Locate every blood parasite and identify its species.
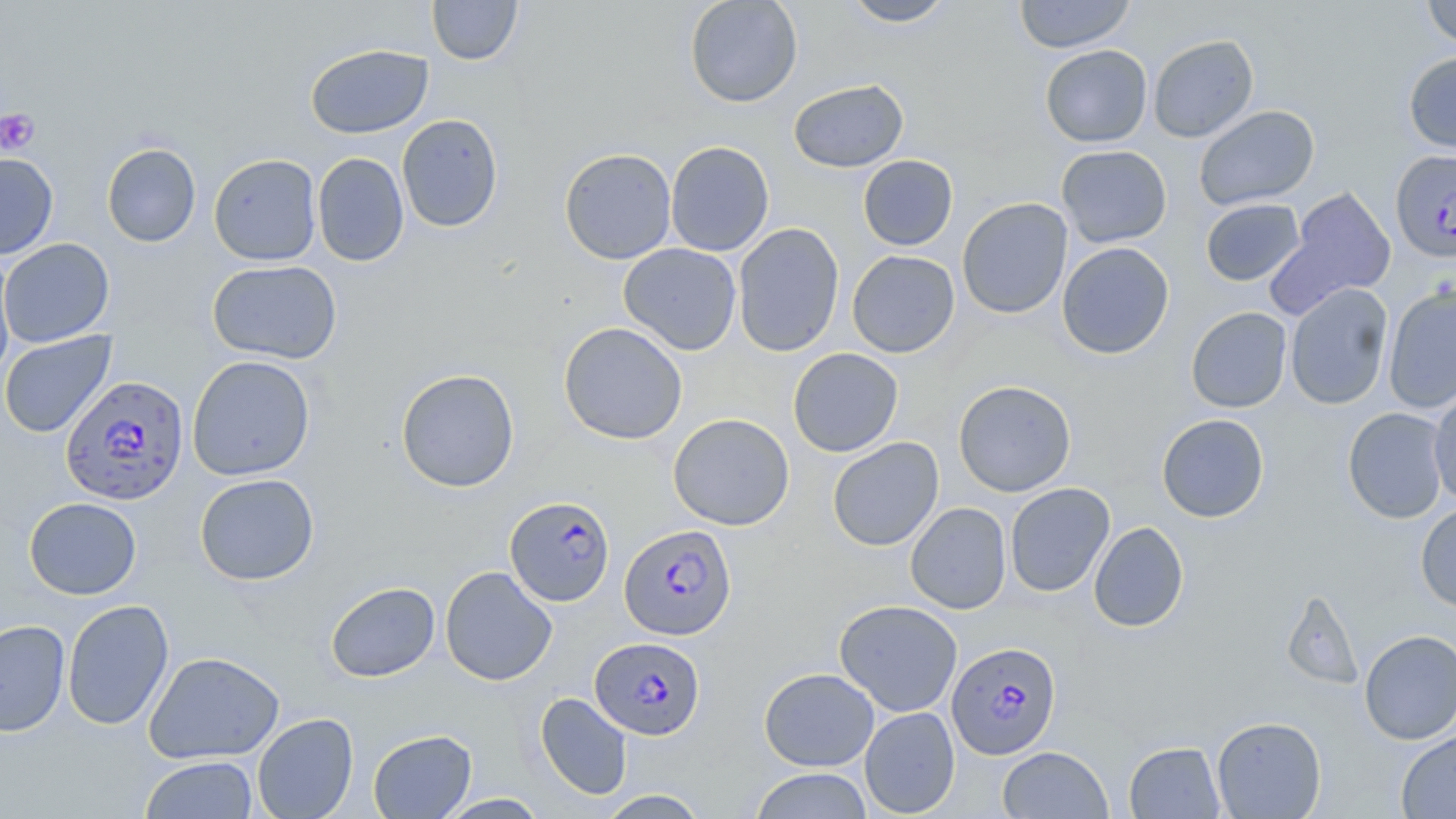
Approximate bounding boxes as [x1, y1, x2, y2] in pixels.
Plasmodium falciparum-infected red blood cells: [1390, 149, 1456, 262], [60, 374, 188, 505], [505, 495, 616, 606], [619, 524, 736, 640], [589, 638, 706, 741], [946, 641, 1062, 760].
No Plasmodium ovale, Plasmodium malariae, Plasmodium vivax, Babesia divergens, or Trypanosoma brucei observed.

Uninfected red blood cell locations: [427, 0, 523, 65], [684, 0, 803, 108], [841, 0, 957, 27], [1013, 0, 1136, 53], [1421, 0, 1456, 49], [1148, 34, 1259, 143], [304, 44, 434, 139], [1040, 44, 1152, 148], [1403, 51, 1456, 153], [788, 79, 909, 173], [1194, 105, 1320, 211], [396, 113, 504, 233], [665, 140, 775, 257], [101, 143, 201, 247], [1056, 144, 1172, 248], [559, 147, 677, 264], [0, 152, 59, 260], [312, 152, 409, 267], [208, 153, 322, 265], [858, 155, 958, 251], [1269, 186, 1397, 316], [957, 197, 1073, 319], [1200, 198, 1305, 286], [732, 222, 845, 357], [0, 238, 114, 347], [1057, 242, 1175, 359], [618, 243, 742, 355], [0, 249, 17, 384], [846, 250, 960, 358], [207, 259, 342, 364], [1284, 283, 1393, 410], [1383, 285, 1456, 414], [1186, 307, 1292, 413], [558, 322, 688, 445], [0, 331, 117, 438], [788, 348, 903, 457], [187, 355, 315, 480], [395, 368, 520, 492], [953, 380, 1076, 497], [1427, 390, 1456, 506], [1342, 407, 1450, 523], [668, 413, 795, 530], [1156, 413, 1269, 523], [827, 437, 944, 551], [194, 473, 319, 585], [1004, 482, 1115, 597], [24, 497, 142, 600], [905, 502, 1012, 614], [1415, 502, 1456, 612], [1089, 521, 1188, 632], [440, 566, 557, 686], [325, 581, 440, 682], [1281, 590, 1364, 691], [62, 599, 174, 731], [834, 599, 962, 717], [0, 619, 70, 737], [1359, 629, 1456, 744], [144, 651, 285, 764], [759, 667, 879, 770], [535, 692, 632, 800], [859, 706, 960, 818], [252, 712, 359, 819], [1212, 716, 1326, 818], [368, 729, 477, 818], [1396, 730, 1456, 818], [1124, 741, 1226, 818], [997, 746, 1113, 818], [139, 756, 258, 818], [749, 768, 874, 818], [596, 789, 711, 818], [435, 793, 550, 818]. Platelet locations: [0, 108, 40, 156]. Slide-level diagnosis: Plasmodium falciparum. Optical microscopy. Thin blood smear. May-Grünwald-Giemsa-stained preparation. 1000x magnification. Image is 1456×819 pixels. Single field of view.